Identify the parasite.
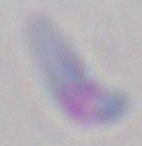
Toxoplasma gondii.

Summary:
  - Magnification: 1000x
  - Modality: photomicrograph